Assess this cell for malaria.
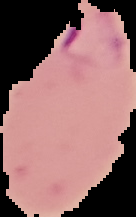
Parasitized.

image type = segmented cell region on a black background
image size = 136×217 pixels
preparation = thin blood film